Classify this cell by malaria status.
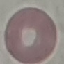
It is uninfected.

Thin blood smear. Automatically extracted cell patch, resized to 64 × 64 pixels. Giemsa-stained preparation. Photographed with a smartphone camera at the microscope eyepiece.